Outline each Plasmodium vivax-infected red blood cell.
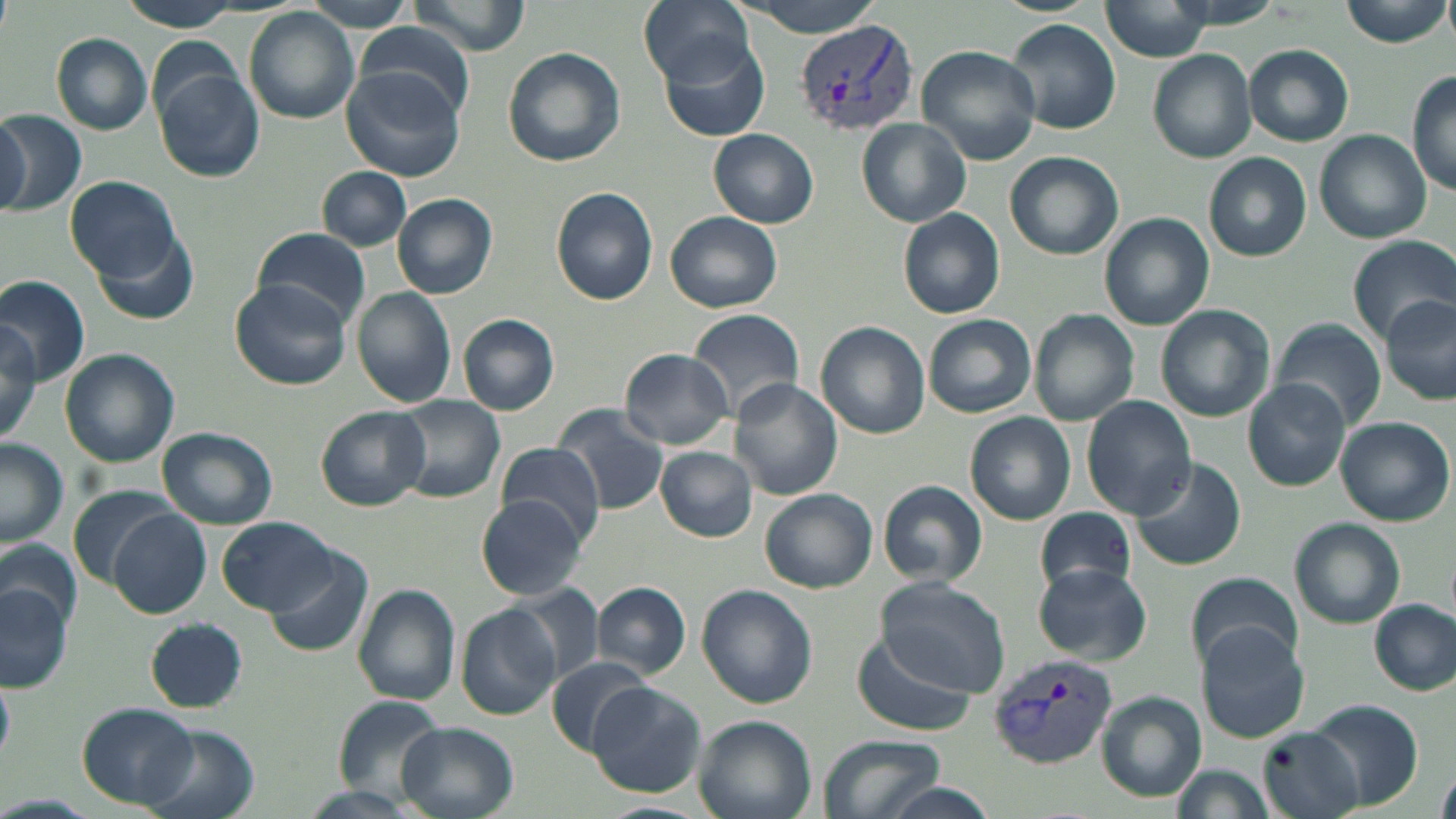
Approximate bounding boxes as (x1, y1, x2, y2) in pixels.
Plasmodium vivax-infected red blood cells: (795, 18, 918, 137), (989, 652, 1118, 769).

slide-level diagnosis = Plasmodium vivax
field of view = one of a larger specimen
image size = 1456×819 pixels
preparation = thin blood smear
modality = optical microscopy
stain = May-Grünwald-Giemsa
uninfected red blood cell locations = approximate bounding boxes as (x1, y1, x2, y2) in pixels: (119, 0, 243, 31), (303, 0, 417, 31), (409, 0, 531, 56), (639, 0, 753, 86), (729, 0, 890, 38), (1102, 0, 1212, 60), (1152, 0, 1288, 29), (1341, 0, 1451, 48), (245, 8, 359, 124), (1006, 18, 1122, 135), (355, 21, 477, 123), (51, 33, 153, 136), (660, 36, 771, 143), (1244, 44, 1354, 146), (916, 45, 1041, 166), (502, 47, 627, 168), (1148, 49, 1257, 163), (153, 65, 265, 184), (340, 66, 467, 184), (1407, 70, 1456, 194), (1, 111, 86, 216), (0, 112, 30, 213), (859, 119, 970, 225), (709, 129, 818, 229), (1314, 130, 1432, 243), (1004, 151, 1123, 259), (1204, 152, 1311, 261), (319, 167, 411, 249), (66, 176, 180, 282), (551, 186, 659, 305), (393, 194, 498, 299), (898, 207, 1005, 319), (664, 211, 784, 313), (1099, 213, 1212, 330), (86, 225, 203, 326), (252, 228, 370, 324), (1346, 237, 1456, 347), (0, 274, 91, 382), (231, 280, 351, 387), (350, 287, 457, 408), (1383, 294, 1456, 402), (1155, 303, 1276, 422), (688, 308, 805, 422), (1029, 311, 1139, 426), (923, 313, 1036, 420), (458, 314, 559, 415), (0, 322, 43, 449), (816, 322, 930, 439), (1273, 322, 1386, 429), (619, 348, 734, 449), (60, 349, 179, 467), (728, 378, 843, 501), (1243, 380, 1351, 490), (391, 395, 505, 504), (1082, 396, 1197, 518), (553, 405, 668, 514), (316, 406, 431, 510), (966, 412, 1076, 526), (1336, 416, 1453, 526), (156, 426, 278, 530), (0, 440, 68, 548), (494, 443, 608, 544), (655, 446, 757, 541), (1130, 458, 1247, 571), (879, 478, 987, 587), (68, 486, 176, 585), (761, 488, 877, 593), (475, 496, 591, 602), (1034, 506, 1136, 597), (108, 509, 212, 618), (219, 516, 336, 614), (1290, 517, 1405, 628), (0, 540, 78, 637), (265, 545, 374, 657), (1033, 563, 1152, 665), (1185, 572, 1300, 675), (0, 579, 72, 693), (877, 579, 1008, 696), (591, 582, 691, 677), (352, 584, 461, 704), (697, 584, 816, 708), (509, 585, 606, 686), (1370, 601, 1453, 694), (457, 604, 560, 719), (145, 618, 246, 713), (1196, 625, 1312, 742), (851, 629, 978, 737), (543, 658, 657, 753), (0, 674, 15, 763), (587, 682, 706, 798), (1098, 693, 1206, 801), (329, 696, 447, 801), (1310, 699, 1424, 808), (78, 703, 199, 810), (693, 714, 816, 819), (396, 723, 518, 818), (138, 725, 260, 819), (1260, 727, 1366, 819), (820, 733, 942, 819), (1167, 764, 1276, 819), (1438, 765, 1456, 819), (295, 783, 427, 819), (881, 784, 999, 819), (592, 801, 712, 819)
magnification = 1000x